Name the cell type shown.
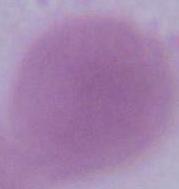

An erythrocyte.

Summary:
  - Modality: photomicrograph
  - Magnification: 1000x